Comment on the morphology of the red blood cells.
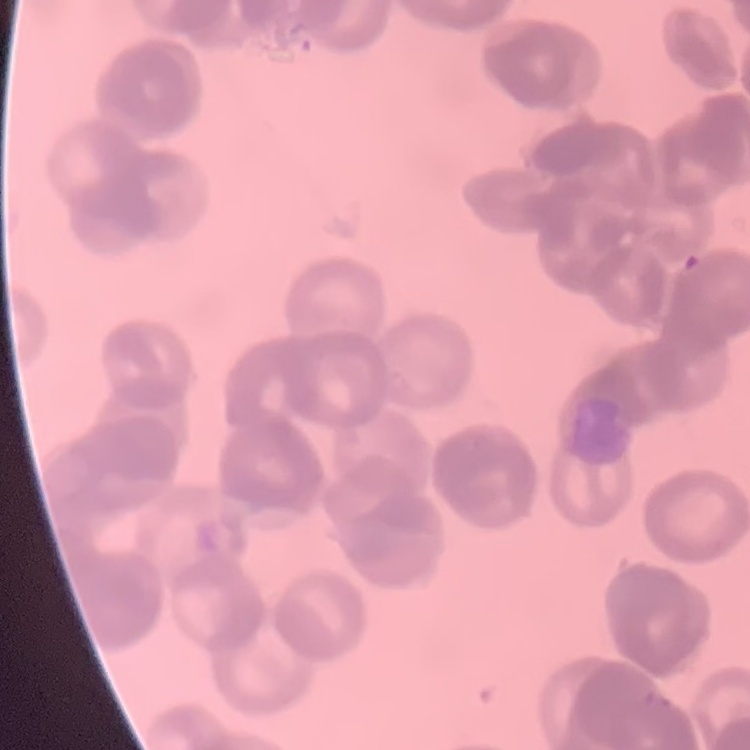

Rouleaux formation.

Summary:
  - Stain: Field's or Giemsa
  - Image type: one tile cut from a larger photomicrograph
  - Preparation: thin blood film